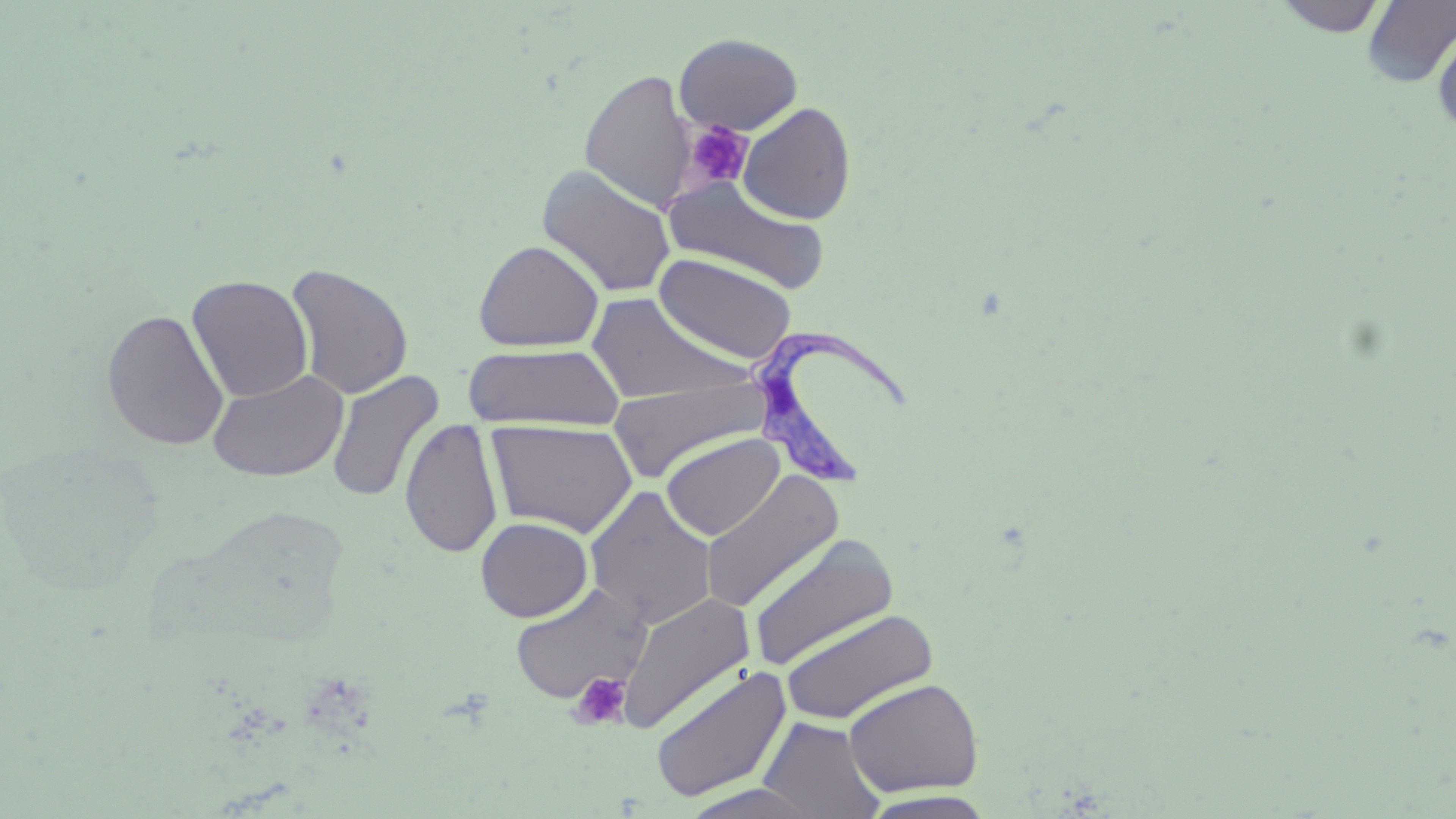
Summary:
  - Coordinate format: approximate bounding boxes as (x1, y1, x2, y2) in pixels
  - Uninfected red blood cell locations: (1274, 0, 1388, 38), (1362, 1, 1456, 87), (1432, 20, 1456, 136), (674, 32, 803, 135), (580, 69, 694, 210), (738, 102, 857, 224), (536, 164, 677, 297), (661, 174, 831, 294), (473, 239, 604, 353), (654, 252, 798, 363), (285, 262, 414, 400), (186, 274, 314, 403), (586, 292, 752, 407), (101, 307, 230, 451), (462, 343, 625, 431), (207, 368, 348, 482), (326, 370, 444, 503), (608, 372, 770, 484), (400, 417, 503, 558), (486, 419, 638, 538), (661, 432, 785, 541), (0, 437, 168, 593), (700, 469, 845, 613), (584, 486, 718, 628), (475, 516, 593, 621), (747, 533, 900, 672), (509, 581, 654, 705), (616, 591, 755, 735), (779, 607, 940, 726), (649, 664, 791, 803), (842, 677, 984, 797), (758, 715, 887, 817), (678, 783, 829, 818), (856, 790, 1000, 818)
  - Trypanosoma brucei locations: (747, 321, 913, 489)
  - Platelet locations: (682, 120, 753, 192), (569, 671, 632, 731)
  - Slide-level diagnosis: Trypanosoma brucei
  - Stain: May-Grünwald-Giemsa
  - Magnification: 1000x
  - Image size: 1456×819 pixels
  - Preparation: thin blood film
  - Modality: optical microscopy
  - Field of view: single